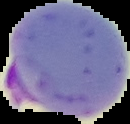
From a thin blood smear. Cell region segmented out of the field of view; the surrounding area is masked to black. Malaria status: parasitized. Image is 130×124 pixels.